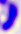

Summary:
  - Identification: Toxoplasma gondii
  - Modality: micrograph
  - Magnification: 400x